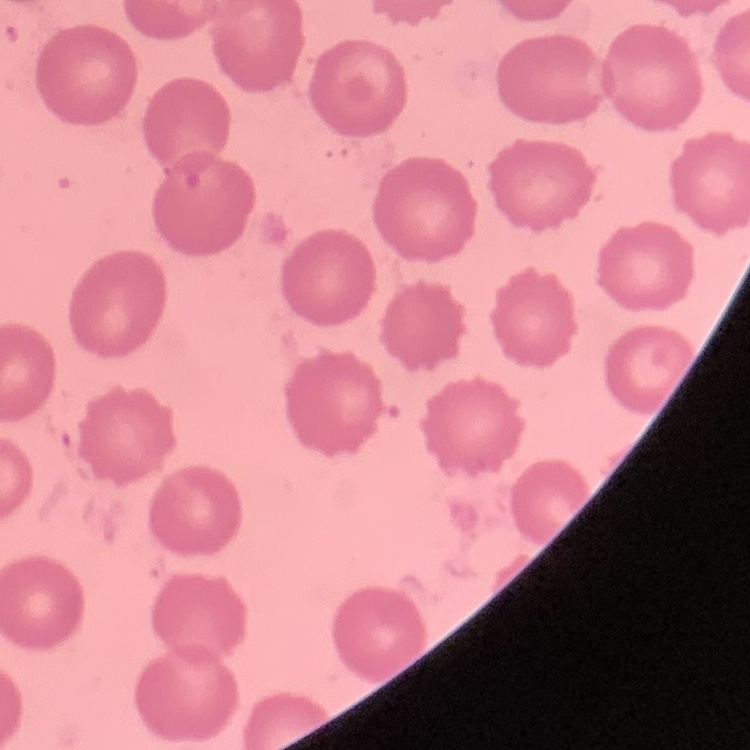 The red blood cells show no rouleaux formation. Thin blood smear. Field's or Giemsa stain. One tile cut from a larger photomicrograph.